Give the position of every malaria parasite.
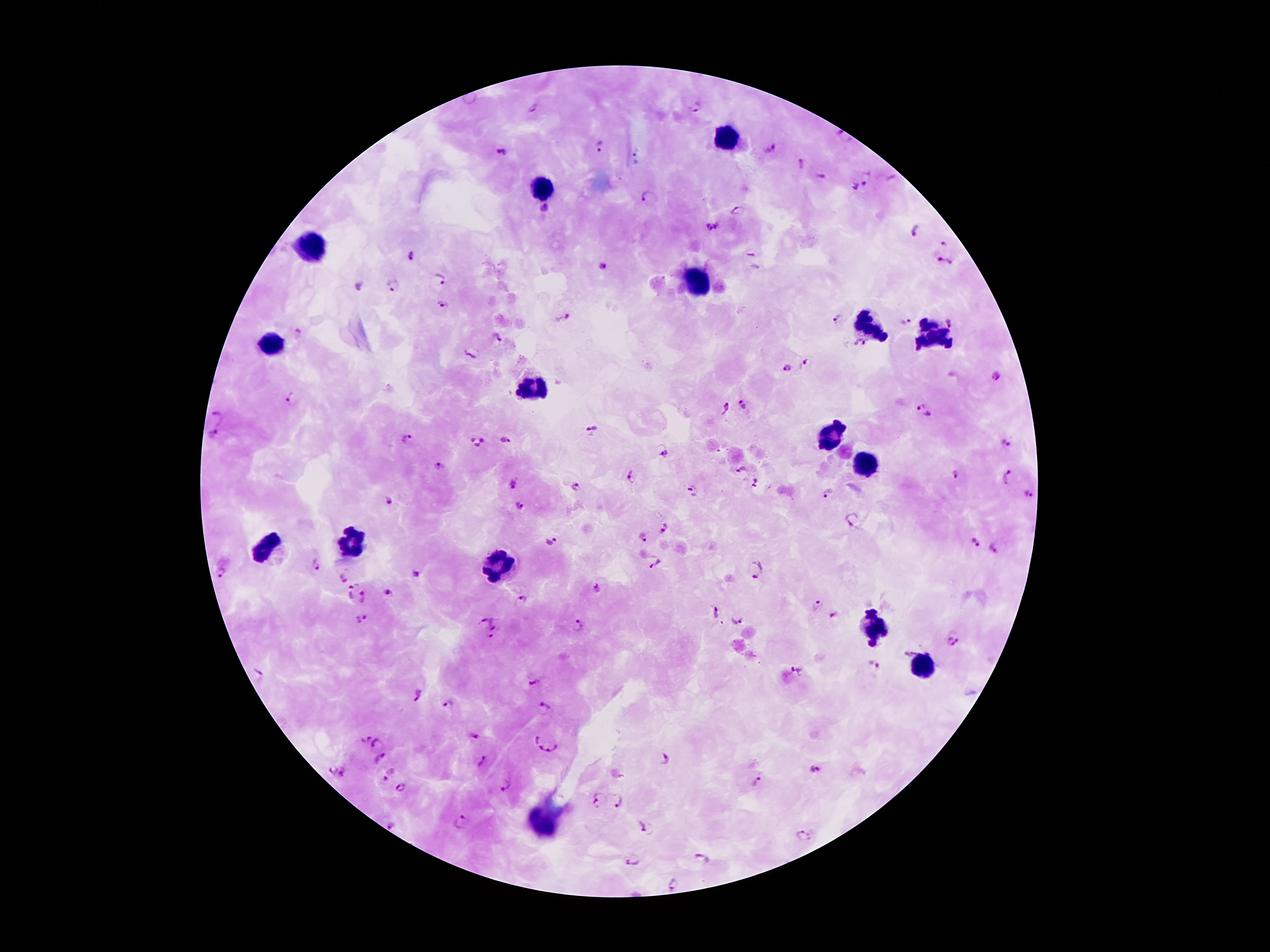

Approximate object centers, in pixels from the top-left corner.
Malaria parasites: (x=697, y=107), (x=532, y=109), (x=840, y=136), (x=601, y=145), (x=772, y=149), (x=502, y=151), (x=802, y=164), (x=820, y=175), (x=868, y=179), (x=853, y=187), (x=648, y=198), (x=546, y=209), (x=739, y=212), (x=711, y=226), (x=915, y=230), (x=945, y=244), (x=410, y=255), (x=943, y=262), (x=604, y=267), (x=440, y=280), (x=394, y=287), (x=442, y=305), (x=562, y=318), (x=837, y=319), (x=951, y=321), (x=906, y=322), (x=298, y=333), (x=497, y=339), (x=860, y=343), (x=471, y=354), (x=805, y=362), (x=787, y=368), (x=997, y=377), (x=291, y=400), (x=743, y=404), (x=726, y=409), (x=923, y=412), (x=217, y=417), (x=592, y=432), (x=213, y=434), (x=408, y=438), (x=506, y=440), (x=478, y=443), (x=1005, y=444), (x=663, y=454), (x=437, y=466), (x=740, y=470), (x=958, y=474), (x=632, y=475), (x=1007, y=478), (x=756, y=482), (x=515, y=487), (x=577, y=488), (x=694, y=491), (x=827, y=494), (x=1027, y=496), (x=390, y=500), (x=520, y=506), (x=853, y=519), (x=663, y=529), (x=643, y=539), (x=551, y=540), (x=975, y=543), (x=993, y=548), (x=654, y=562), (x=315, y=565), (x=756, y=568), (x=223, y=572), (x=416, y=574), (x=342, y=575), (x=597, y=588), (x=350, y=590), (x=388, y=592), (x=365, y=596), (x=522, y=600), (x=814, y=603), (x=716, y=613), (x=835, y=615), (x=363, y=619), (x=737, y=619), (x=485, y=625), (x=497, y=625), (x=578, y=625), (x=491, y=637), (x=951, y=642), (x=909, y=653), (x=874, y=664), (x=796, y=670), (x=258, y=677), (x=535, y=681), (x=419, y=695), (x=449, y=704), (x=544, y=707), (x=475, y=735), (x=367, y=739), (x=537, y=739), (x=377, y=743), (x=549, y=746), (x=665, y=758), (x=379, y=759), (x=482, y=761), (x=332, y=769), (x=815, y=769), (x=344, y=773), (x=389, y=774), (x=617, y=774), (x=757, y=782), (x=505, y=786), (x=400, y=787), (x=599, y=801), (x=619, y=801), (x=461, y=823), (x=393, y=825), (x=644, y=827), (x=803, y=836), (x=701, y=858), (x=633, y=861), (x=674, y=884).

Summary:
  - Leukocyte locations: (x=725, y=135), (x=543, y=187), (x=313, y=248), (x=704, y=284), (x=869, y=325), (x=931, y=336), (x=270, y=347), (x=536, y=389), (x=831, y=436), (x=864, y=462), (x=354, y=539), (x=270, y=550), (x=497, y=566), (x=871, y=623), (x=923, y=663), (x=543, y=824)
  - Magnification: 100x
  - Stain: Giemsa
  - Capture: smartphone through the microscope eyepiece
  - Patient malaria status: infected with Plasmodium falciparum
  - Field of view: single
  - Preparation: thick blood smear
  - Image size: 1270×952 pixels